Evaluate for malaria.
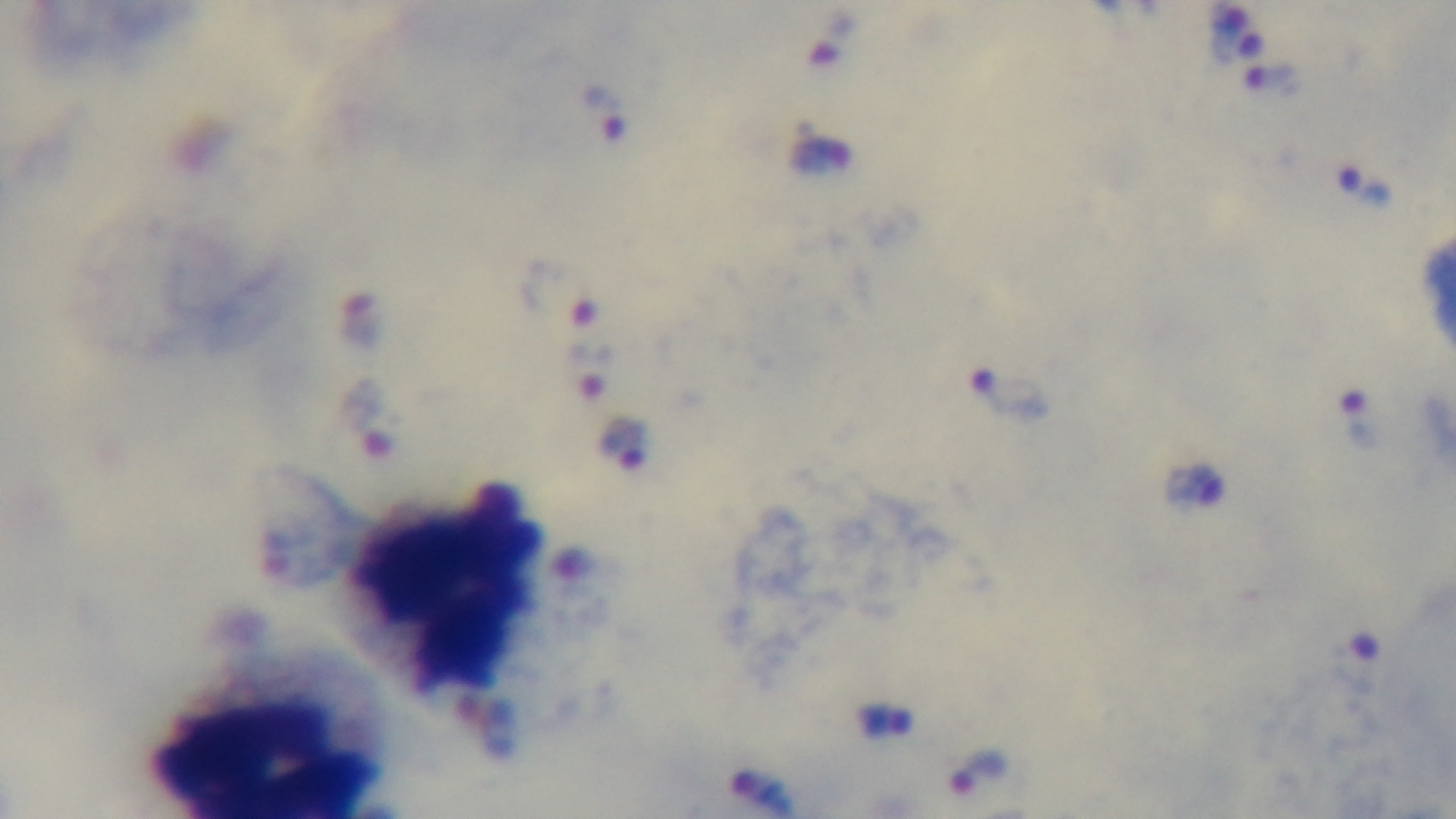

It is infected.

Summary:
  - Preparation: thick blood film
  - Stain: Giemsa
  - Field of view: one from the slide
  - Capture: mounted 4K digital camera
  - Modality: light microscopy
  - Objective: 100x oil immersion